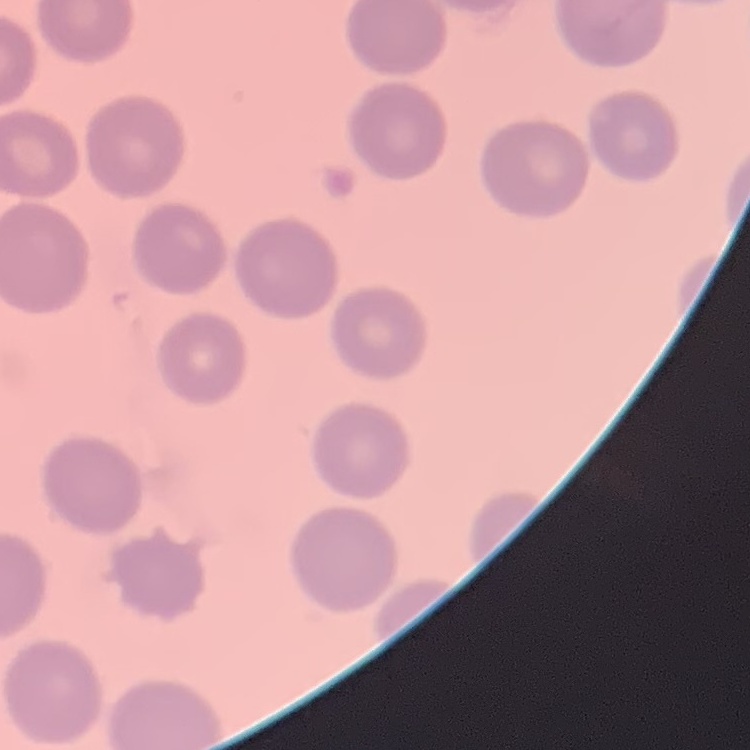
Summary:
  - Erythrocyte morphology: no rouleaux formation
  - Preparation: thin peripheral smear
  - Image type: square crop of a larger photomicrograph
  - Stain: Field's or Giemsa